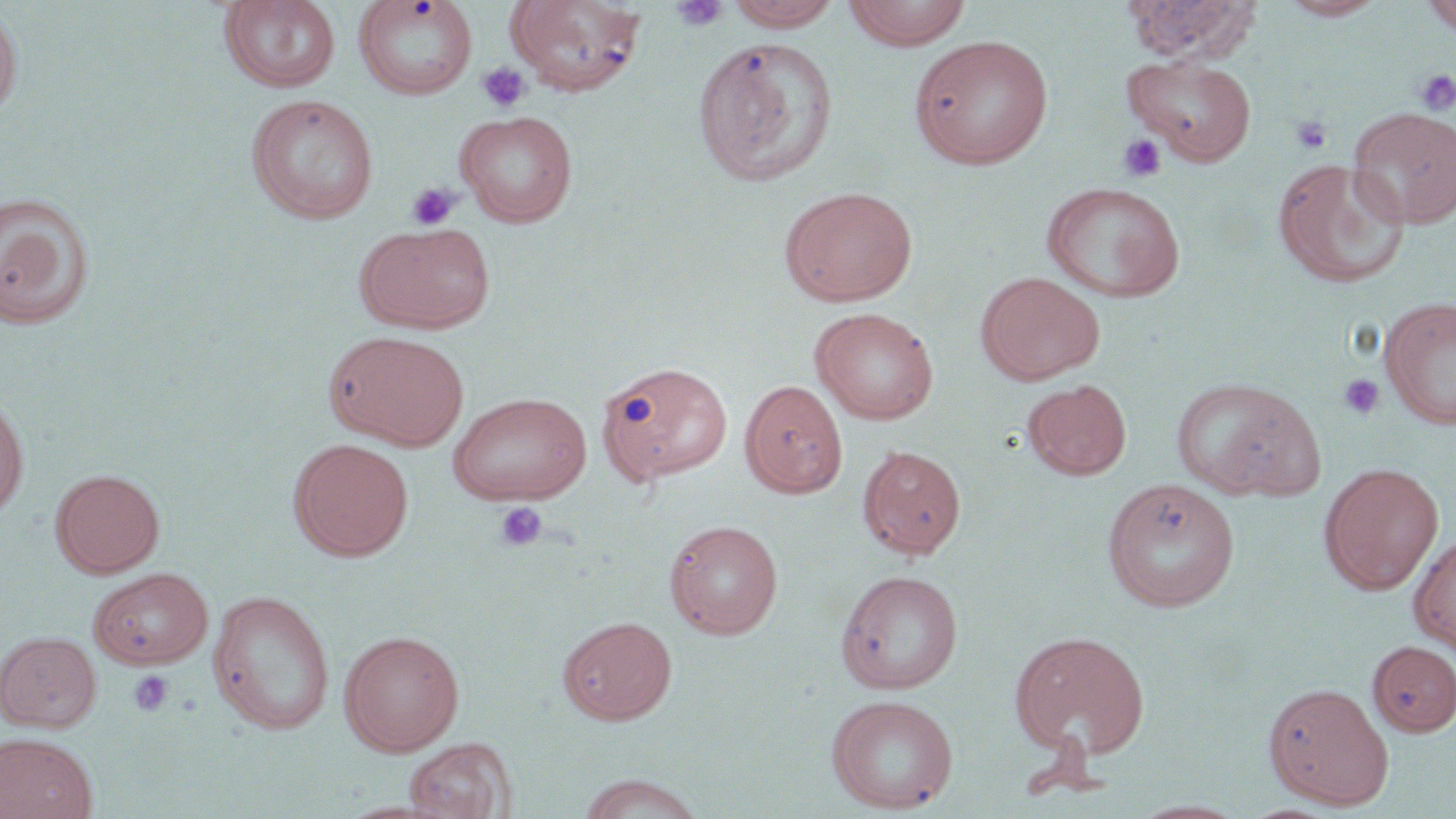

Summary:
  - Coordinate format: approximate bounding boxes as named x1/y1/x2/y2 corners in pixels
  - Platelet locations: (x1=669, y1=0, x2=729, y2=32), (x1=477, y1=62, x2=531, y2=112), (x1=1414, y1=69, x2=1456, y2=116), (x1=1289, y1=114, x2=1333, y2=155), (x1=1117, y1=134, x2=1166, y2=183), (x1=407, y1=183, x2=460, y2=230), (x1=1338, y1=373, x2=1384, y2=421), (x1=493, y1=501, x2=549, y2=552), (x1=129, y1=670, x2=173, y2=717)
  - Uninfected red blood cell locations: (x1=352, y1=0, x2=478, y2=100), (x1=505, y1=0, x2=648, y2=96), (x1=724, y1=0, x2=842, y2=31), (x1=842, y1=0, x2=973, y2=50), (x1=1122, y1=0, x2=1262, y2=64), (x1=1277, y1=0, x2=1388, y2=20), (x1=1419, y1=0, x2=1456, y2=36), (x1=218, y1=1, x2=342, y2=95), (x1=0, y1=4, x2=23, y2=123), (x1=908, y1=35, x2=1055, y2=169), (x1=692, y1=37, x2=838, y2=187), (x1=1122, y1=54, x2=1258, y2=165), (x1=245, y1=94, x2=379, y2=224), (x1=1347, y1=107, x2=1456, y2=229), (x1=454, y1=109, x2=579, y2=227), (x1=1272, y1=158, x2=1411, y2=290), (x1=1040, y1=181, x2=1187, y2=302), (x1=779, y1=185, x2=919, y2=307), (x1=0, y1=191, x2=97, y2=331), (x1=355, y1=223, x2=495, y2=334), (x1=975, y1=271, x2=1105, y2=384), (x1=1379, y1=296, x2=1456, y2=430), (x1=810, y1=307, x2=939, y2=425), (x1=325, y1=331, x2=470, y2=451), (x1=596, y1=360, x2=734, y2=485), (x1=1171, y1=377, x2=1322, y2=501), (x1=1022, y1=378, x2=1131, y2=480), (x1=740, y1=380, x2=847, y2=498), (x1=448, y1=392, x2=593, y2=506), (x1=0, y1=395, x2=29, y2=518), (x1=288, y1=437, x2=414, y2=561), (x1=858, y1=444, x2=966, y2=559), (x1=1319, y1=462, x2=1444, y2=595), (x1=50, y1=468, x2=165, y2=578), (x1=1101, y1=478, x2=1240, y2=612), (x1=664, y1=519, x2=783, y2=639), (x1=1408, y1=534, x2=1456, y2=654), (x1=88, y1=567, x2=213, y2=670), (x1=835, y1=569, x2=964, y2=694), (x1=207, y1=589, x2=336, y2=735), (x1=557, y1=616, x2=677, y2=725), (x1=339, y1=629, x2=464, y2=756), (x1=0, y1=630, x2=102, y2=733), (x1=1010, y1=630, x2=1150, y2=760), (x1=1368, y1=640, x2=1456, y2=737), (x1=1263, y1=681, x2=1394, y2=808), (x1=826, y1=694, x2=958, y2=814), (x1=0, y1=733, x2=98, y2=819), (x1=404, y1=736, x2=516, y2=818), (x1=575, y1=772, x2=708, y2=819), (x1=1130, y1=799, x2=1249, y2=818)
  - Slide-level diagnosis: negative for blood parasites
  - Field of view: one of a larger specimen
  - Image size: 1456×819 pixels
  - Modality: light microscopy
  - Stain: May-Grünwald-Giemsa
  - Magnification: 1000x
  - Preparation: thin blood film